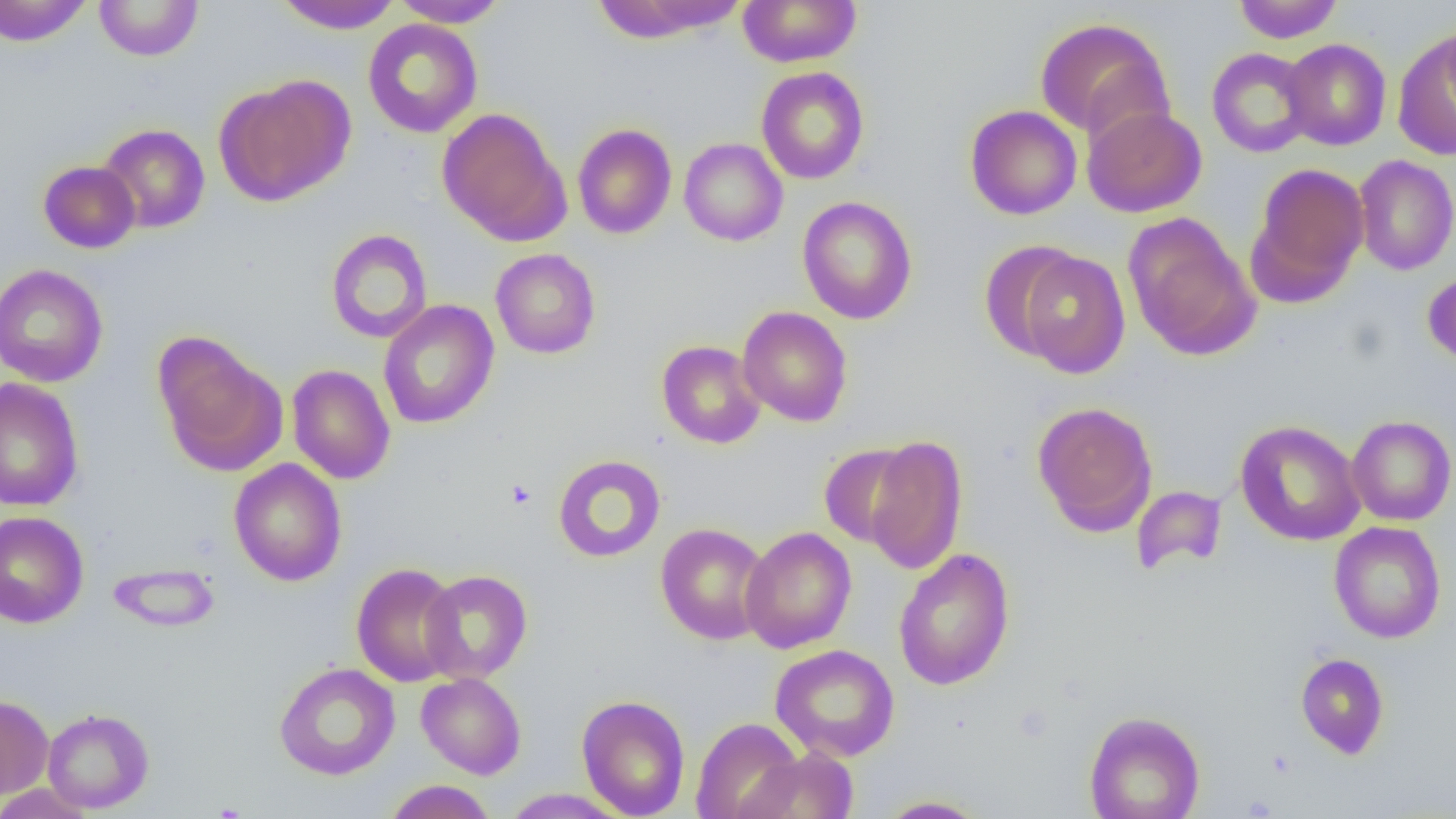 Approximate bounding boxes as [x1, y1, x2, y2] in pixels. Platelet locations: [505, 479, 536, 509]. Uninfected red blood cell locations: [0, 0, 93, 47], [274, 0, 402, 34], [391, 0, 509, 27], [738, 0, 861, 68], [1233, 0, 1343, 44], [94, 1, 204, 61], [591, 1, 747, 42], [1034, 17, 1175, 144], [362, 18, 483, 139], [1439, 18, 1456, 120], [1394, 32, 1456, 160], [1281, 38, 1391, 151], [1206, 48, 1315, 158], [756, 66, 869, 185], [214, 75, 355, 206], [965, 105, 1082, 220], [1082, 106, 1207, 217], [437, 108, 568, 245], [572, 123, 677, 239], [97, 124, 210, 233], [679, 138, 788, 246], [1353, 154, 1456, 275], [38, 160, 141, 253], [1247, 162, 1370, 303], [797, 196, 918, 324], [1123, 213, 1260, 361], [325, 228, 433, 344], [979, 241, 1084, 362], [490, 248, 601, 359], [1013, 249, 1132, 378], [0, 263, 108, 388], [1423, 271, 1456, 368], [377, 300, 500, 429], [737, 306, 853, 427], [153, 335, 287, 477], [656, 340, 766, 449], [286, 364, 396, 485], [0, 377, 84, 511], [1031, 401, 1158, 535], [1346, 415, 1455, 526], [1235, 419, 1365, 546], [864, 436, 968, 574], [818, 442, 920, 548], [552, 455, 666, 563], [228, 458, 347, 586], [1131, 485, 1227, 576], [0, 511, 89, 628], [1329, 521, 1446, 644], [655, 522, 772, 645], [740, 526, 857, 653], [893, 548, 1015, 691], [107, 562, 220, 632], [351, 562, 462, 687], [419, 569, 533, 684], [770, 644, 900, 762], [1295, 653, 1390, 759], [274, 662, 400, 780], [416, 672, 527, 779], [0, 694, 53, 799], [576, 694, 691, 819], [42, 708, 154, 814], [1084, 710, 1205, 819], [691, 717, 805, 819], [735, 747, 858, 818], [383, 780, 497, 818], [0, 783, 96, 819], [501, 788, 630, 818], [876, 796, 992, 818]. Slide-level diagnosis: no evidence of blood parasites. Optical microscopy. Captured at 1000x magnification. One field of a larger specimen. Thin blood film. Image is 1456×819 pixels.